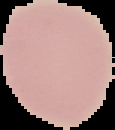
Result: no Plasmodium parasites detected. Cell region segmented out of the field of view; the surrounding area is masked to black. Image is 115×130 pixels. From a thin blood smear.